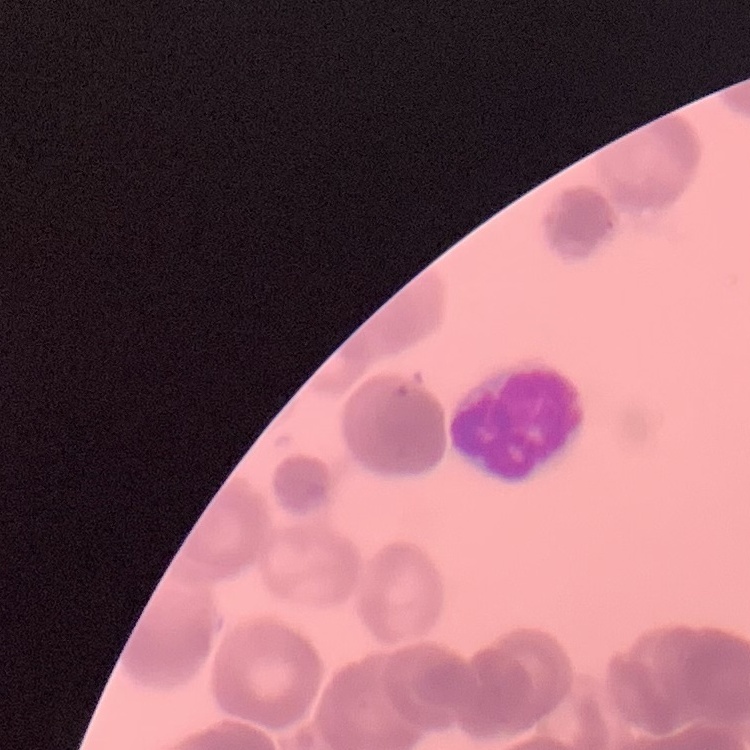
erythrocyte morphology = rouleaux formation
preparation = thin blood smear
stain = Field's or Giemsa
image type = square crop of a larger photomicrograph